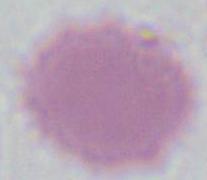

Summary:
  - Magnification: 1000x
  - Identification: red blood cell
  - Modality: photomicrograph